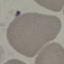
result = no malaria parasites seen
preparation = thin blood film
stain = Giemsa
capture = smartphone through the microscope eyepiece
image type = automatically extracted cell patch, resized to 64 × 64 pixels